Locate every Plasmodium falciparum-infected red blood cell.
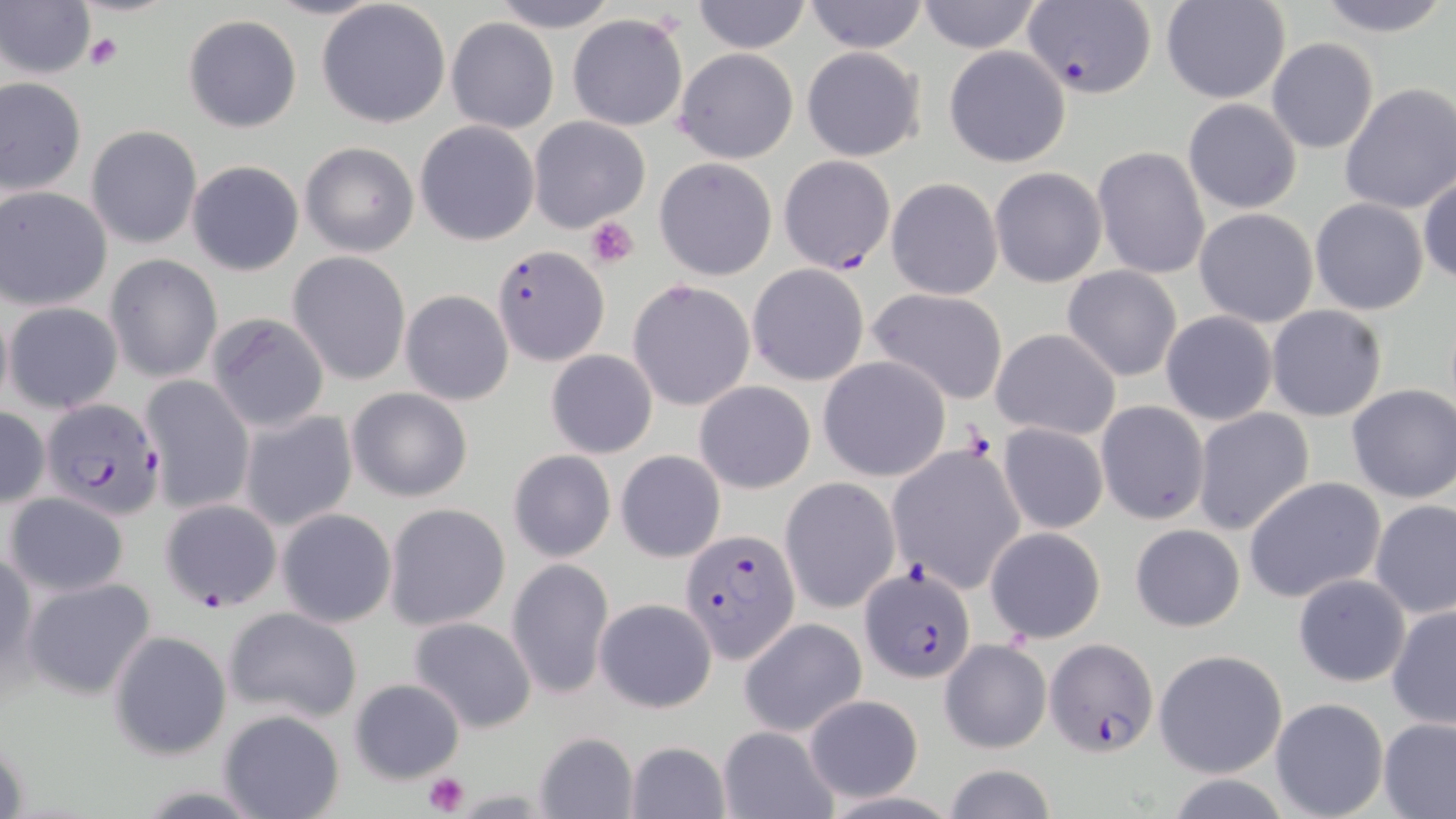

Approximate bounding boxes as [x1, y1, x2, y2] in pixels.
Plasmodium falciparum-infected red blood cells: [1023, 3, 1156, 97], [778, 155, 896, 274], [493, 244, 608, 365], [41, 399, 164, 519], [161, 498, 282, 610], [680, 530, 800, 661], [861, 568, 975, 684], [1043, 637, 1160, 755].

{
  "slide_level_diagnosis": "Plasmodium falciparum",
  "platelet_locations": "approximate bounding boxes as [x1, y1, x2, y2] in pixels: [85, 32, 123, 71], [585, 214, 640, 268], [424, 772, 468, 816]",
  "modality": "light microscopy",
  "magnification": "1000x",
  "preparation": "thin blood film",
  "uninfected_red_blood_cell_locations": "approximate bounding boxes as [x1, y1, x2, y2] in pixels: [487, 0, 621, 32], [691, 0, 812, 53], [801, 0, 930, 53], [1161, 0, 1291, 102], [1312, 0, 1454, 36], [916, 1, 1044, 53], [0, 2, 94, 81], [318, 2, 451, 127], [568, 13, 687, 131], [182, 14, 303, 134], [445, 18, 560, 134], [1266, 38, 1379, 155], [943, 45, 1073, 167], [801, 46, 925, 161], [674, 48, 798, 164], [0, 75, 87, 196], [1339, 83, 1456, 215], [1182, 98, 1301, 213], [528, 116, 650, 232], [414, 119, 541, 246], [85, 125, 202, 249], [299, 140, 420, 258], [1094, 146, 1213, 281], [654, 158, 777, 281], [186, 159, 305, 277], [989, 167, 1106, 287], [1418, 173, 1455, 286], [886, 177, 1003, 300], [1, 186, 112, 311], [1309, 198, 1429, 316], [1194, 207, 1318, 328], [288, 252, 411, 385], [106, 255, 222, 383], [746, 263, 869, 386], [1062, 266, 1182, 382], [628, 279, 755, 411], [868, 287, 1009, 405], [400, 290, 514, 407], [0, 298, 13, 417], [3, 302, 122, 414], [1266, 305, 1388, 422], [1159, 311, 1278, 426], [206, 312, 331, 431], [991, 328, 1121, 441], [545, 348, 658, 459], [817, 356, 950, 482], [139, 375, 254, 514], [694, 381, 815, 494], [1346, 385, 1456, 503], [347, 388, 473, 501], [1095, 401, 1210, 526], [0, 406, 49, 508], [238, 408, 358, 534], [1191, 408, 1315, 538], [996, 423, 1108, 536], [886, 444, 1023, 594], [507, 449, 617, 563], [616, 450, 725, 562], [1244, 475, 1385, 603], [780, 476, 900, 614], [5, 492, 129, 596], [1370, 501, 1456, 620], [383, 502, 511, 631], [276, 508, 397, 629], [1130, 523, 1244, 632], [984, 526, 1106, 643], [0, 543, 36, 689], [506, 559, 614, 699], [1293, 574, 1412, 687], [23, 576, 157, 701], [595, 597, 717, 714], [1386, 604, 1456, 731], [223, 606, 363, 724], [408, 617, 539, 734], [739, 618, 867, 737], [108, 630, 231, 759], [940, 639, 1050, 753], [1154, 649, 1288, 778], [350, 677, 466, 784], [801, 694, 924, 802], [1270, 697, 1389, 819], [218, 708, 346, 819], [1378, 717, 1456, 817], [717, 726, 837, 818], [533, 731, 639, 819], [622, 739, 730, 818], [940, 762, 1057, 819]",
  "image_size": "1456×819 pixels",
  "field_of_view": "one of a larger specimen",
  "stain": "May-Grünwald-Giemsa"
}